Point out each leukocyte.
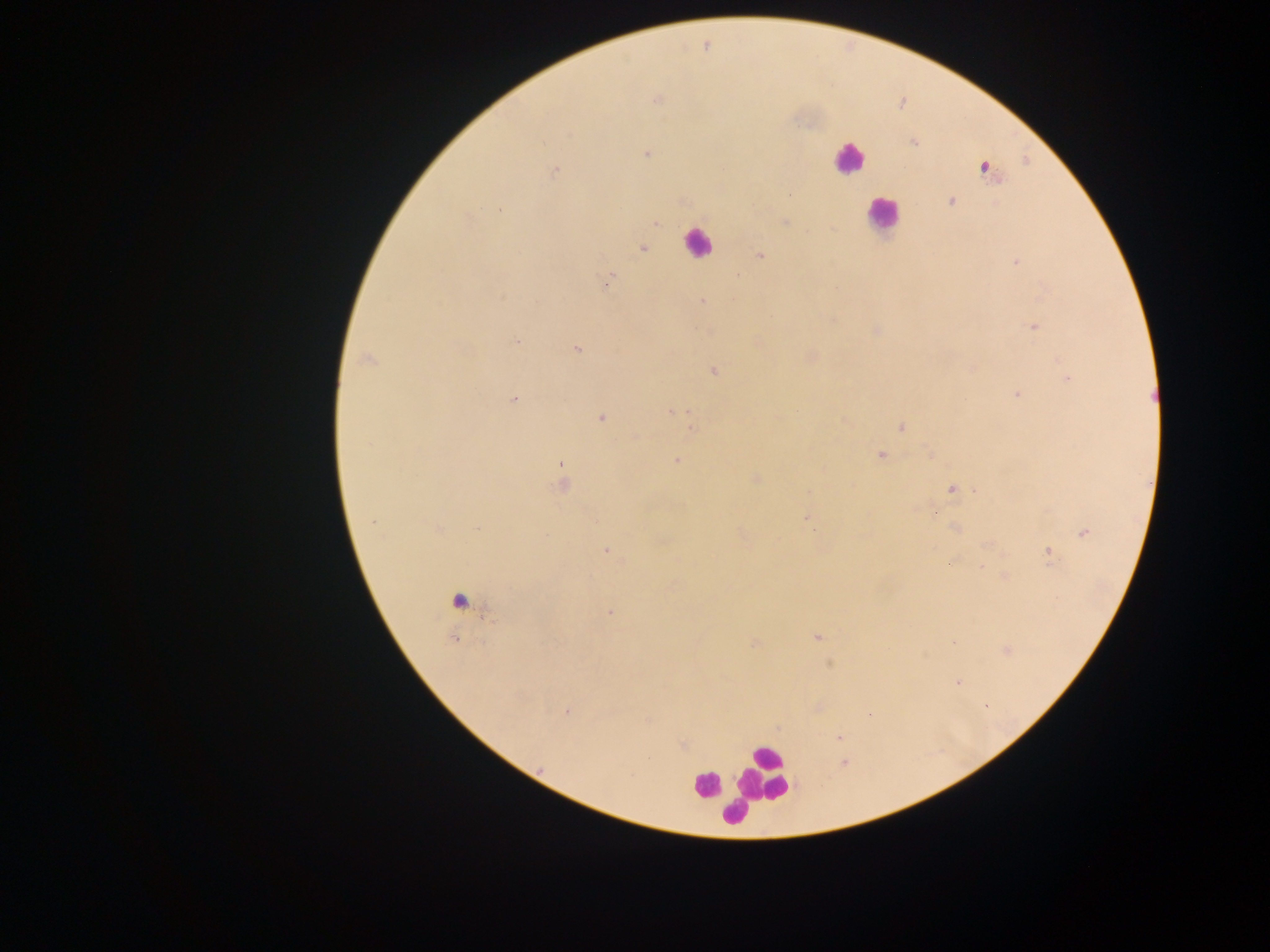
Approximate centers as (x, y) in pixels.
Leukocytes: (848, 158), (881, 215), (697, 243), (458, 596), (765, 772), (705, 786), (733, 812).

capture: mobile-phone photograph through a microscope
field_of_view: single
image_size: 1270×952 pixels
country: Ghana
malaria_parasite_locations: 'approximate centers as (x, y) in pixels: (657, 99), (913, 143), (647, 153), (984, 168), (555, 171), (951, 201), (500, 210), (784, 222), (655, 223), (643, 248), (760, 256), (1015, 262), (606, 283), (702, 301), (1034, 327), (877, 330), (516, 341), (577, 349), (367, 359), (714, 370), (1068, 378), (1017, 396), (514, 399), (671, 411), (600, 418), (693, 428), (901, 428), (881, 455), (676, 461), (561, 463), (757, 478), (562, 485), (952, 490), (934, 512), (805, 517), (373, 522), (955, 528), (439, 529), (478, 529), (1084, 532), (606, 551), (1048, 553), (948, 563), (982, 567), (1005, 576), (610, 612), (817, 637), (755, 643), (958, 682), (985, 706), (566, 713), (869, 714), (840, 738), (843, 762)'
preparation: thick blood film